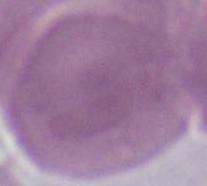

Micrograph. 1000x magnification. An erythrocyte is shown.